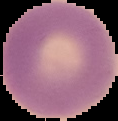
From a thin blood smear. Malaria status: uninfected. Segmented cell region on a black background. Image is 118×121 pixels.